Assess the morphology of the red blood cells.
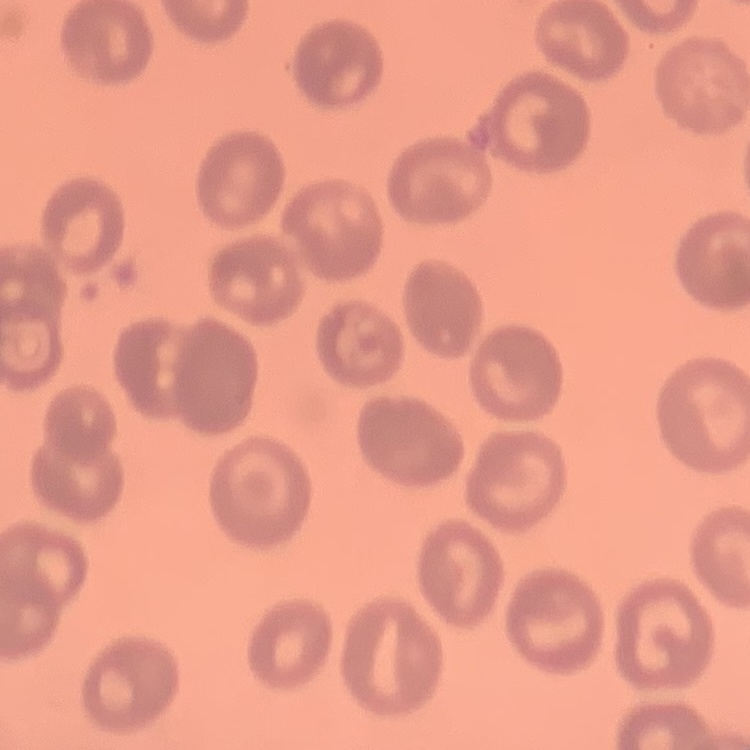

They show no rouleaux formation.

Summary:
  - Stain: Field's or Giemsa
  - Preparation: thin peripheral smear
  - Image type: square crop of a larger photomicrograph